Identify the parasite.
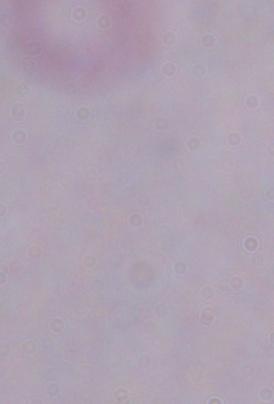

This is a trypanosome.

magnification: 1000x
modality: photomicrograph